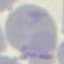

Result: no malaria parasites seen. Thin blood smear. Automatically extracted cell patch, resized to 64 × 64 pixels. Acquired by smartphone through the microscope eyepiece. Giemsa stain.